Assess this cell for malaria.
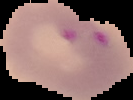

It is parasitized.

Summary:
  - Preparation: thin blood film
  - Image size: 133×100 pixels
  - Image type: segmented cell region with the area outside set to black